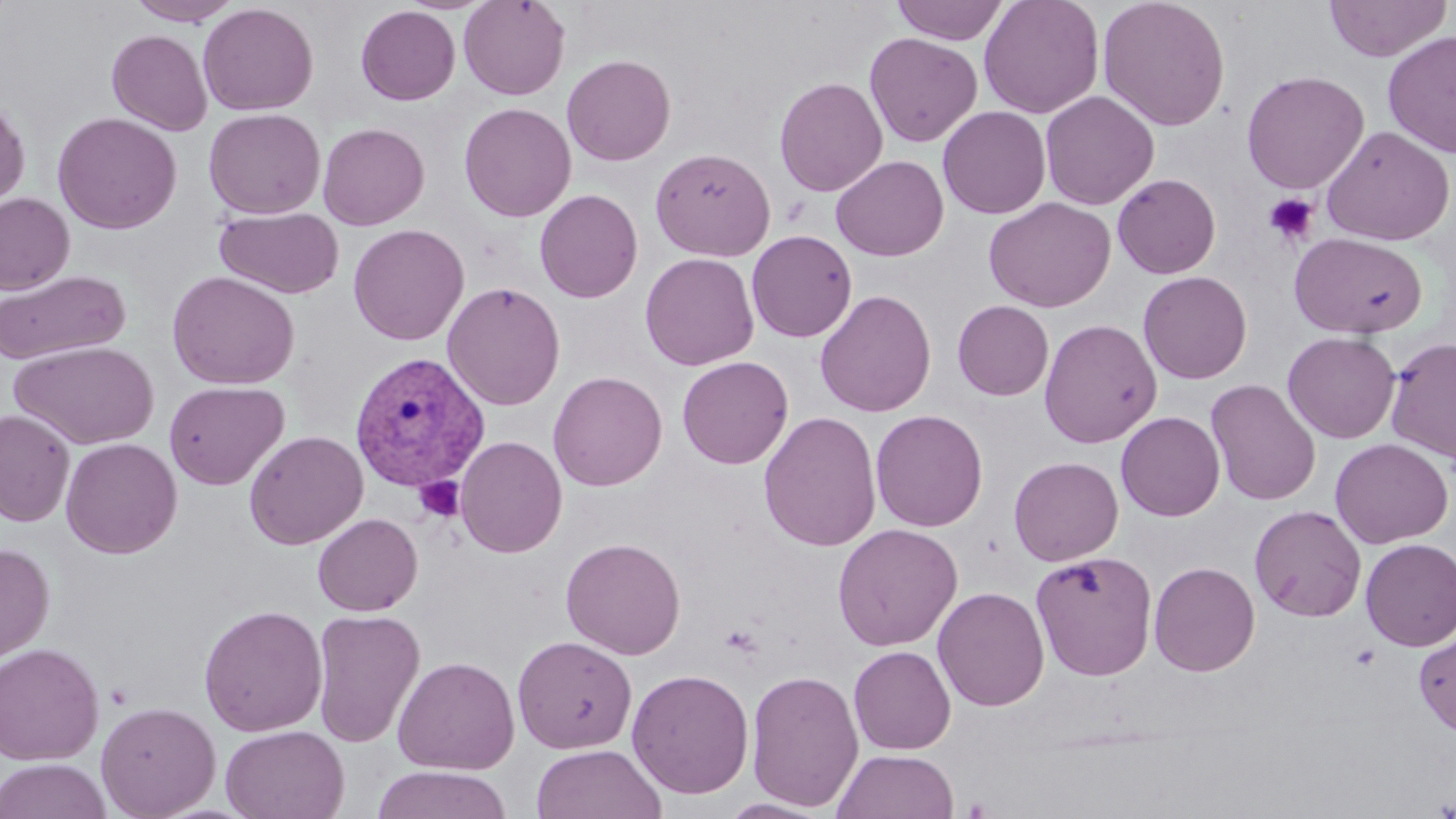

slide-level diagnosis = Plasmodium vivax
magnification = 1000x
Plasmodium vivax-infected red blood cell locations = approximate bounding boxes as named x1/y1/x2/y2 corners in pixels: (x1=349, y1=351, x2=491, y2=492)
platelet locations = approximate bounding boxes as named x1/y1/x2/y2 corners in pixels: (x1=1263, y1=192, x2=1319, y2=245), (x1=414, y1=476, x2=465, y2=522)
field of view = single
image size = 1456×819 pixels
preparation = thin blood smear
modality = light microscopy
stain = May-Grünwald-Giemsa
uninfected red blood cell locations = approximate bounding boxes as named x1/y1/x2/y2 corners in pixels: (x1=127, y1=0, x2=242, y2=26), (x1=458, y1=0, x2=570, y2=100), (x1=890, y1=0, x2=1010, y2=45), (x1=978, y1=0, x2=1104, y2=119), (x1=1097, y1=0, x2=1231, y2=131), (x1=1323, y1=0, x2=1453, y2=62), (x1=198, y1=2, x2=319, y2=116), (x1=356, y1=5, x2=460, y2=105), (x1=106, y1=29, x2=213, y2=135), (x1=1382, y1=31, x2=1456, y2=159), (x1=864, y1=32, x2=983, y2=147), (x1=561, y1=54, x2=676, y2=165), (x1=1241, y1=70, x2=1369, y2=194), (x1=774, y1=77, x2=888, y2=197), (x1=1040, y1=90, x2=1159, y2=210), (x1=0, y1=94, x2=30, y2=212), (x1=459, y1=102, x2=577, y2=222), (x1=938, y1=106, x2=1051, y2=218), (x1=203, y1=108, x2=326, y2=219), (x1=52, y1=112, x2=182, y2=234), (x1=317, y1=122, x2=430, y2=230), (x1=1321, y1=126, x2=1455, y2=246), (x1=955, y1=131, x2=1096, y2=253), (x1=650, y1=147, x2=775, y2=261), (x1=831, y1=155, x2=948, y2=261), (x1=1112, y1=173, x2=1221, y2=279), (x1=534, y1=189, x2=643, y2=303), (x1=0, y1=193, x2=74, y2=295), (x1=984, y1=197, x2=1116, y2=313), (x1=215, y1=206, x2=345, y2=299), (x1=347, y1=224, x2=469, y2=345), (x1=746, y1=230, x2=858, y2=342), (x1=1289, y1=231, x2=1429, y2=338), (x1=640, y1=252, x2=760, y2=371), (x1=0, y1=269, x2=130, y2=365), (x1=167, y1=270, x2=301, y2=390), (x1=1138, y1=271, x2=1252, y2=384), (x1=442, y1=281, x2=565, y2=411), (x1=814, y1=289, x2=937, y2=417), (x1=952, y1=300, x2=1054, y2=401), (x1=1039, y1=318, x2=1162, y2=448), (x1=1282, y1=331, x2=1401, y2=443), (x1=1385, y1=336, x2=1456, y2=464), (x1=10, y1=340, x2=160, y2=451), (x1=676, y1=356, x2=794, y2=469), (x1=548, y1=370, x2=668, y2=492), (x1=1206, y1=378, x2=1321, y2=506), (x1=163, y1=380, x2=290, y2=490), (x1=0, y1=409, x2=75, y2=526), (x1=870, y1=409, x2=988, y2=532), (x1=758, y1=410, x2=882, y2=552), (x1=1115, y1=411, x2=1225, y2=521), (x1=244, y1=430, x2=369, y2=549), (x1=455, y1=435, x2=568, y2=558), (x1=60, y1=437, x2=183, y2=559), (x1=1330, y1=438, x2=1453, y2=548), (x1=1008, y1=456, x2=1123, y2=565), (x1=414, y1=477, x2=469, y2=520), (x1=1249, y1=505, x2=1367, y2=622), (x1=313, y1=512, x2=423, y2=616), (x1=832, y1=523, x2=963, y2=651), (x1=560, y1=537, x2=686, y2=659), (x1=1359, y1=538, x2=1456, y2=651), (x1=0, y1=542, x2=55, y2=666), (x1=1030, y1=550, x2=1158, y2=680), (x1=1149, y1=561, x2=1260, y2=676), (x1=933, y1=586, x2=1050, y2=711), (x1=198, y1=604, x2=328, y2=736), (x1=310, y1=609, x2=426, y2=747), (x1=1414, y1=627, x2=1456, y2=739), (x1=513, y1=635, x2=637, y2=754), (x1=0, y1=642, x2=105, y2=765), (x1=849, y1=645, x2=956, y2=755), (x1=392, y1=655, x2=520, y2=775), (x1=626, y1=668, x2=754, y2=799), (x1=746, y1=668, x2=864, y2=812), (x1=96, y1=700, x2=221, y2=818), (x1=220, y1=724, x2=349, y2=819), (x1=531, y1=744, x2=667, y2=819), (x1=833, y1=749, x2=959, y2=819), (x1=0, y1=758, x2=112, y2=819), (x1=372, y1=765, x2=513, y2=819), (x1=719, y1=798, x2=834, y2=818)